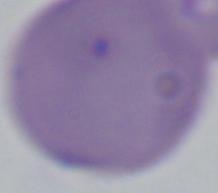
magnification = 1000x
modality = micrograph
identification = Babesia